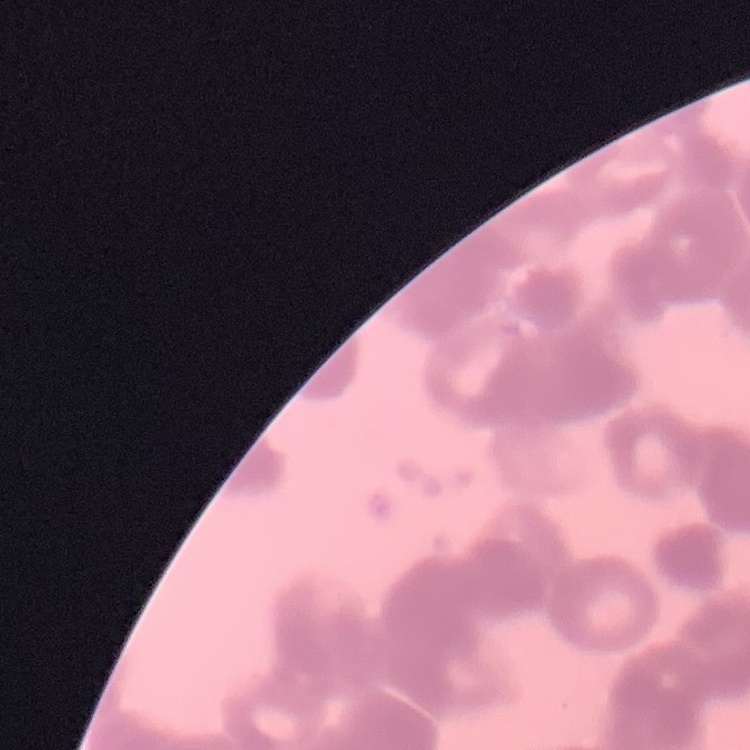
{
  "red_blood_cell_morphology": "rouleaux formation",
  "preparation": "thin peripheral smear",
  "stain": "Field's or Giemsa",
  "image_type": "one tile cut from a larger photomicrograph"
}